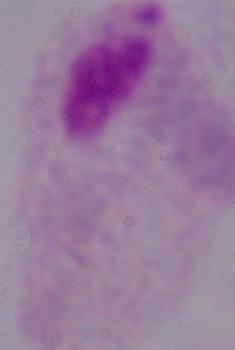
A trichomonad is seen. Micrograph. 1000x magnification.